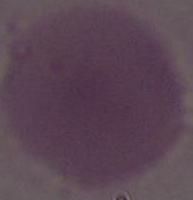
{
  "identification": "red blood cell",
  "modality": "micrograph",
  "magnification": "1000x"
}